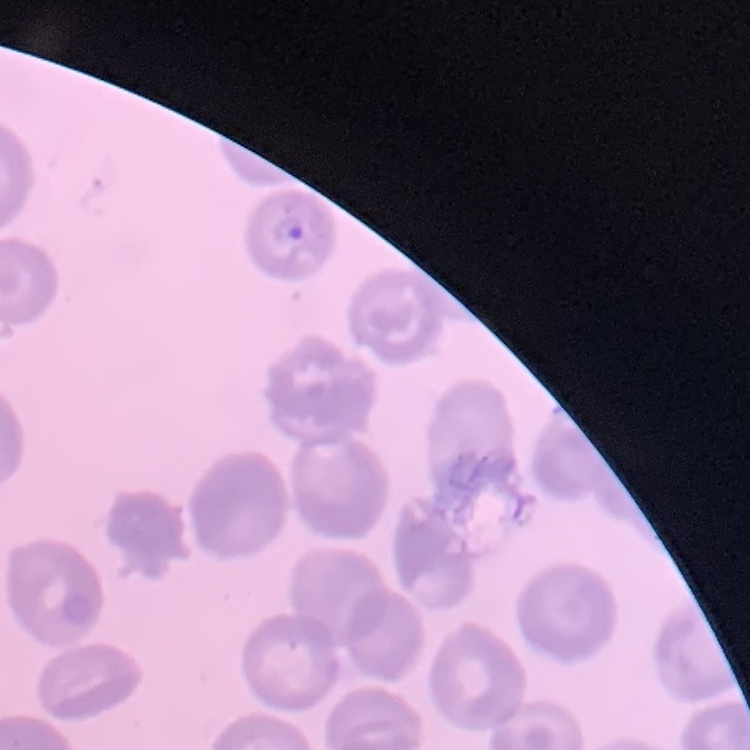 The erythrocytes show no rouleaux formation. Stained with either Field's or Giemsa. Square crop of a larger photomicrograph. Thin blood smear.